Locate every blood parasite and identify its species.
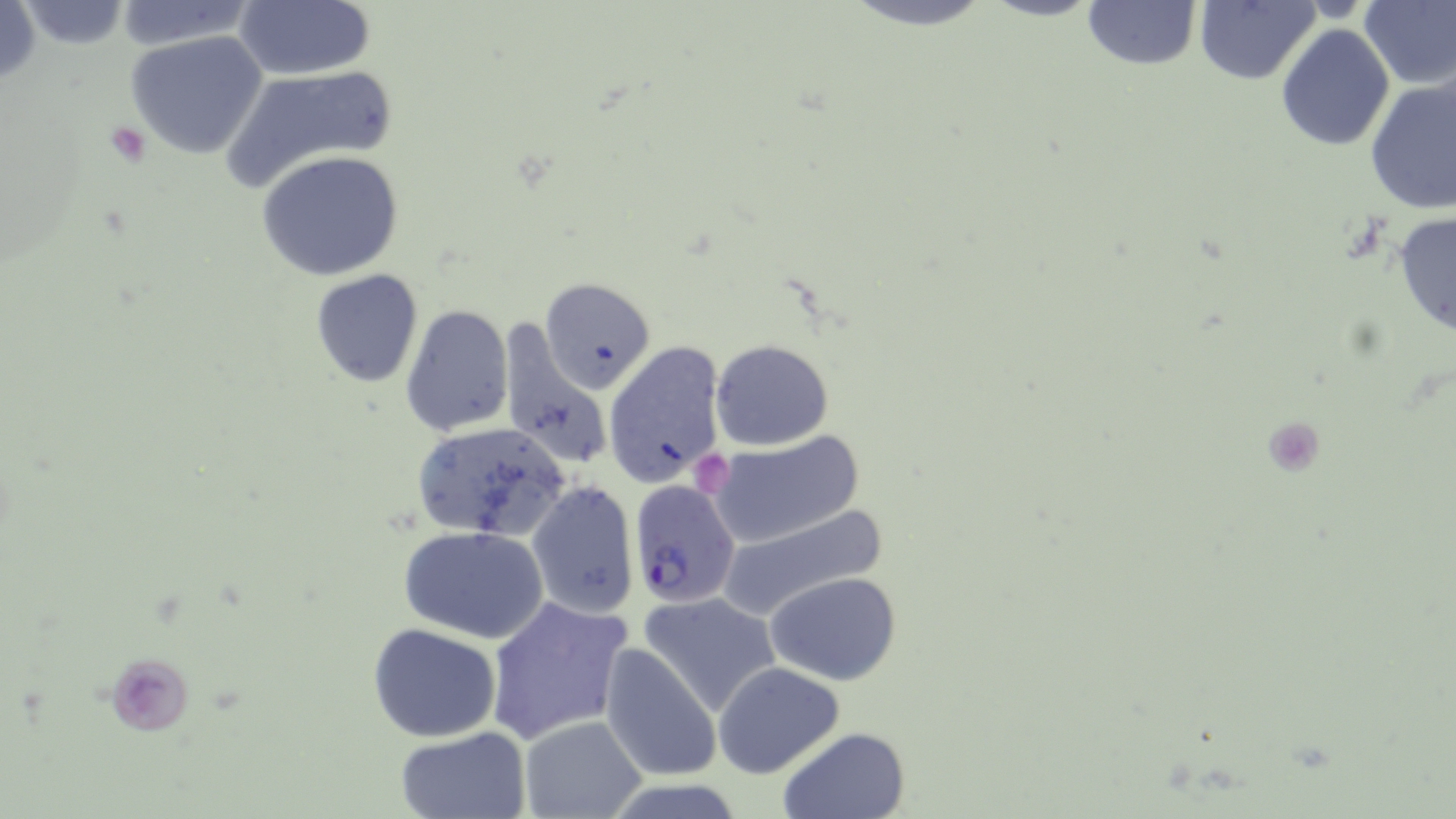

Approximate bounding boxes as (x1, y1, x2, y2) in pixels.
Plasmodium falciparum-infected red blood cells: (628, 481, 742, 608).
No Plasmodium ovale, Plasmodium malariae, Plasmodium vivax, Babesia divergens, or Trypanosoma brucei observed.

Platelet locations: (106, 120, 151, 165), (694, 452, 732, 489), (108, 654, 195, 734). Uninfected red blood cell locations: (837, 0, 1001, 30), (1081, 0, 1201, 72), (1358, 0, 1456, 88), (232, 1, 374, 81), (1192, 2, 1319, 83), (1277, 24, 1394, 150), (125, 30, 269, 159), (224, 65, 396, 191), (1364, 74, 1456, 214), (257, 150, 405, 282), (1392, 210, 1456, 342), (312, 269, 423, 387), (540, 279, 655, 392), (401, 305, 514, 436), (496, 322, 611, 472), (711, 339, 833, 449), (603, 342, 726, 488), (409, 421, 572, 542), (703, 433, 865, 548), (528, 480, 638, 617), (715, 502, 890, 621), (398, 525, 551, 643), (764, 572, 902, 684), (639, 592, 781, 718), (484, 596, 633, 745), (367, 623, 502, 742), (601, 643, 722, 782), (714, 662, 843, 778), (518, 715, 648, 819), (393, 726, 531, 817), (775, 726, 913, 819). Slide-level diagnosis: Plasmodium falciparum. May-Grünwald-Giemsa stain. Thin blood smear. Image is 1456×819 pixels. Optical microscopy. One field of a larger specimen. 1000x magnification.